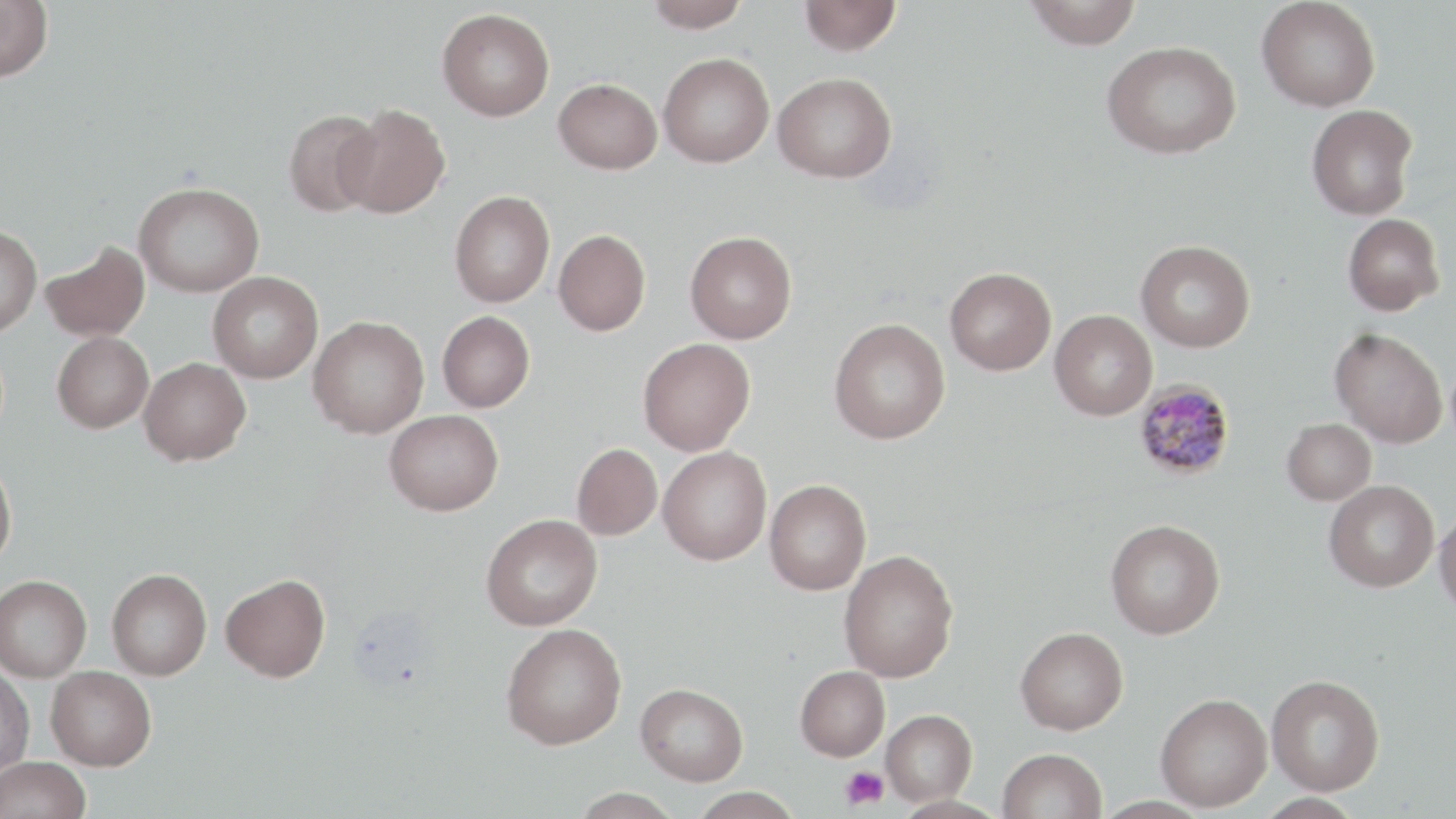

Summary:
  - Coordinate format: approximate bounding boxes as [x1, y1, x2, y2] in pixels
  - Platelet locations: [839, 765, 889, 811]
  - Uninfected red blood cell locations: [0, 0, 53, 82], [643, 0, 752, 32], [799, 0, 902, 56], [1025, 0, 1142, 50], [1256, 0, 1381, 112], [437, 8, 555, 121], [1102, 40, 1241, 159], [658, 52, 774, 167], [773, 72, 897, 182], [554, 78, 662, 174], [338, 104, 451, 218], [1306, 104, 1417, 220], [283, 109, 382, 218], [133, 181, 264, 297], [449, 190, 555, 307], [1343, 213, 1444, 315], [0, 225, 42, 335], [553, 230, 651, 335], [685, 231, 797, 343], [41, 240, 149, 342], [1136, 240, 1255, 352], [945, 267, 1056, 376], [208, 271, 324, 383], [1050, 309, 1157, 420], [437, 311, 534, 412], [308, 315, 429, 438], [829, 318, 950, 444], [1330, 328, 1448, 448], [52, 332, 154, 433], [638, 338, 755, 456], [139, 357, 251, 465], [384, 409, 503, 515], [1282, 418, 1376, 504], [572, 443, 662, 540], [658, 447, 772, 565], [0, 459, 17, 572], [765, 479, 871, 595], [1323, 479, 1439, 592], [1434, 509, 1456, 619], [481, 513, 602, 630], [1105, 519, 1225, 639], [839, 549, 958, 682], [107, 568, 212, 680], [221, 573, 330, 682], [0, 574, 92, 682], [500, 623, 627, 749], [1015, 626, 1128, 734], [795, 665, 890, 761], [0, 666, 35, 776], [46, 666, 157, 770], [1266, 674, 1385, 795], [635, 683, 748, 785], [1155, 692, 1272, 812], [881, 709, 977, 806], [998, 748, 1107, 819], [0, 756, 91, 819], [689, 787, 804, 819], [568, 788, 682, 818]
  - Plasmodium malariae-infected red blood cell locations: [1134, 380, 1236, 481]
  - Slide-level diagnosis: Plasmodium malariae
  - Magnification: 1000x
  - Image size: 1456×819 pixels
  - Preparation: thin blood film
  - Field of view: one of a larger specimen
  - Stain: May-Grünwald-Giemsa
  - Modality: optical microscopy